Outline each blood parasite and name the species.
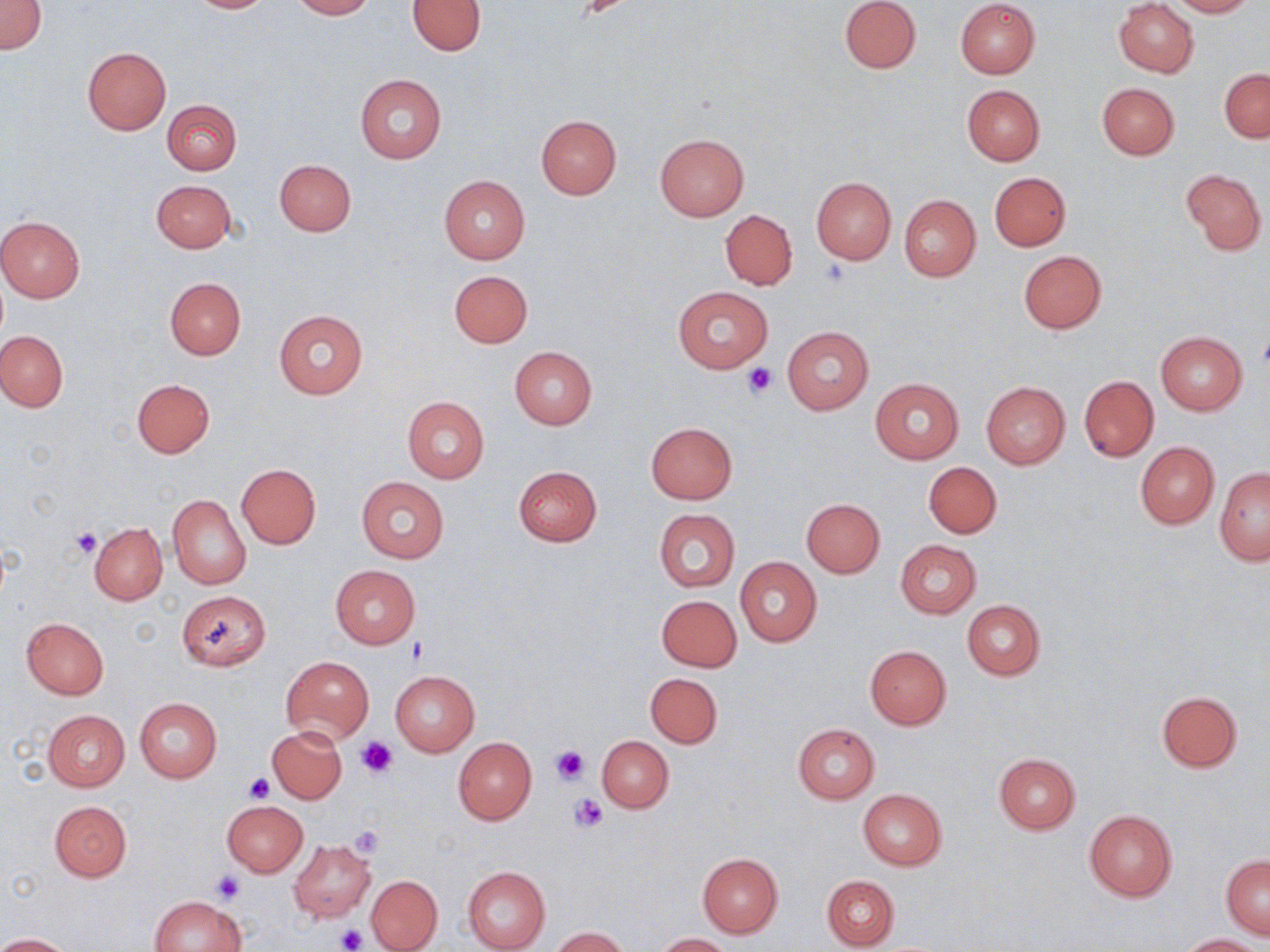

No blood parasites observed.

Approximate bounding boxes as (x1,y1)-(x2,y2) corner pairs in pixels. Platelet locations: (576,1)-(629,20), (819,259)-(851,288), (743,361)-(777,397), (72,527)-(101,558), (405,636)-(428,663), (357,737)-(399,778), (551,744)-(588,785), (242,773)-(273,803), (568,792)-(607,832), (348,825)-(385,859), (212,871)-(243,904), (334,924)-(369,952). Uninfected red blood cell locations: (0,0)-(45,53), (186,0)-(275,13), (291,0)-(375,19), (408,0)-(486,55), (839,0)-(920,74), (955,0)-(1040,80), (1167,0)-(1254,17), (1113,1)-(1198,77), (81,47)-(172,136), (1219,67)-(1269,143), (355,75)-(446,163), (1097,82)-(1180,159), (962,85)-(1045,165), (163,99)-(243,174), (536,115)-(621,199), (654,133)-(748,220), (274,159)-(356,236), (1181,167)-(1267,255), (989,172)-(1071,251), (439,176)-(530,263), (811,176)-(896,263), (151,180)-(236,253), (899,194)-(981,281), (720,210)-(797,289), (0,215)-(86,302), (1018,250)-(1106,333), (447,269)-(533,347), (164,277)-(246,359), (673,285)-(774,373), (273,308)-(368,400), (782,326)-(873,414), (0,330)-(68,411), (1155,331)-(1249,414), (509,346)-(598,428), (1079,375)-(1158,461), (131,378)-(215,457), (870,378)-(964,463), (981,381)-(1070,468), (402,396)-(490,484), (646,421)-(737,504), (1135,442)-(1219,528), (924,462)-(1002,538), (236,464)-(321,548), (514,465)-(603,547), (1215,467)-(1269,564), (356,475)-(450,563), (167,495)-(251,588), (802,498)-(885,577), (654,509)-(740,591), (89,522)-(167,605), (894,539)-(981,618), (735,557)-(822,646), (331,565)-(421,647), (176,590)-(271,671), (657,595)-(741,672), (962,600)-(1046,680), (21,618)-(109,698), (864,645)-(951,730), (282,656)-(373,744), (390,670)-(479,757), (645,672)-(722,748), (1156,691)-(1243,772), (135,698)-(221,783), (42,709)-(129,791), (792,723)-(880,803), (267,726)-(347,804), (596,736)-(672,813), (453,737)-(536,825), (993,753)-(1081,833), (858,789)-(947,869), (222,800)-(308,876), (50,801)-(132,881), (1084,810)-(1178,901), (288,840)-(376,922), (697,852)-(784,937), (1221,853)-(1269,938), (462,866)-(551,952), (821,873)-(900,950), (366,875)-(442,951), (152,895)-(246,951), (550,927)-(632,952), (0,933)-(73,952), (653,933)-(734,951), (1175,934)-(1262,951). Slide-level diagnosis: no evidence of blood parasites. Thin blood film. 1000x magnification. Image is 1270×952 pixels. May-Grünwald-Giemsa-stained preparation. Optical microscopy. Single field of view.